Report the malaria status of this cell.
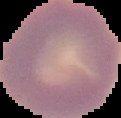

Uninfected.

image type = segmented cell region with the area outside set to black
image size = 121×118 pixels
preparation = thin blood film